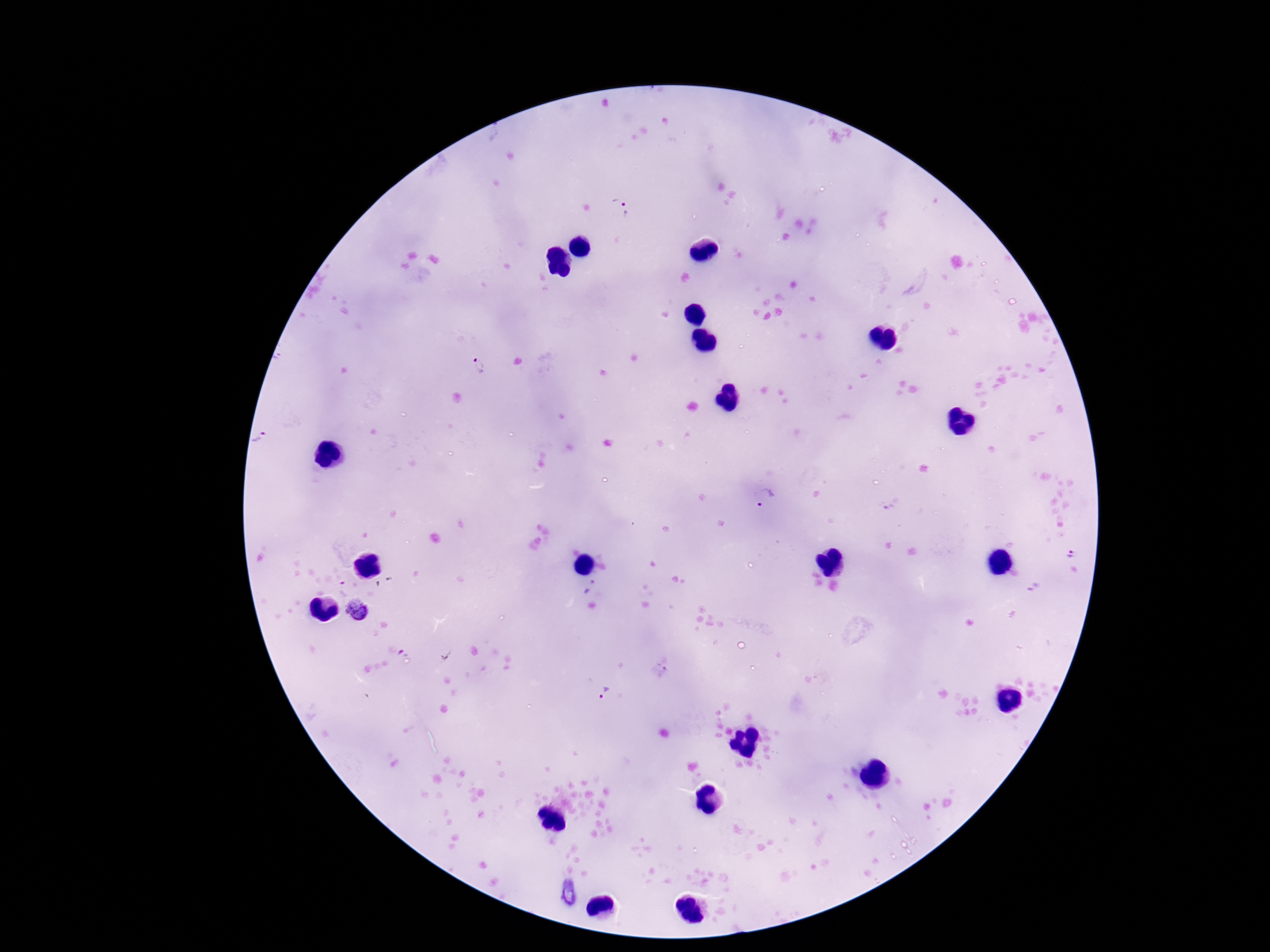

image size = 1270×952 pixels
capture = smartphone camera through the microscope eyepiece
magnification = 100x
Plasmodium parasite locations = approximate centers as (x, y) in pixels: (620, 211), (478, 368), (260, 438), (764, 497), (1072, 552), (589, 588), (357, 610), (604, 694)
field of view = single
patient malaria status = positive
stain = Giemsa
preparation = thick peripheral-blood smear